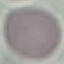
Summary:
  - Result: no malaria parasites detected
  - Stain: Giemsa
  - Capture: smartphone camera at the microscope eyepiece
  - Image type: automatically extracted cell patch, resized to 64 × 64 pixels
  - Preparation: thin blood film